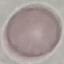

result = no malaria parasites seen
capture = smartphone through the microscope eyepiece
preparation = thin blood smear
stain = Giemsa
image type = automatically extracted cell patch, resized to 64 × 64 pixels